Point out each Plasmodium parasite.
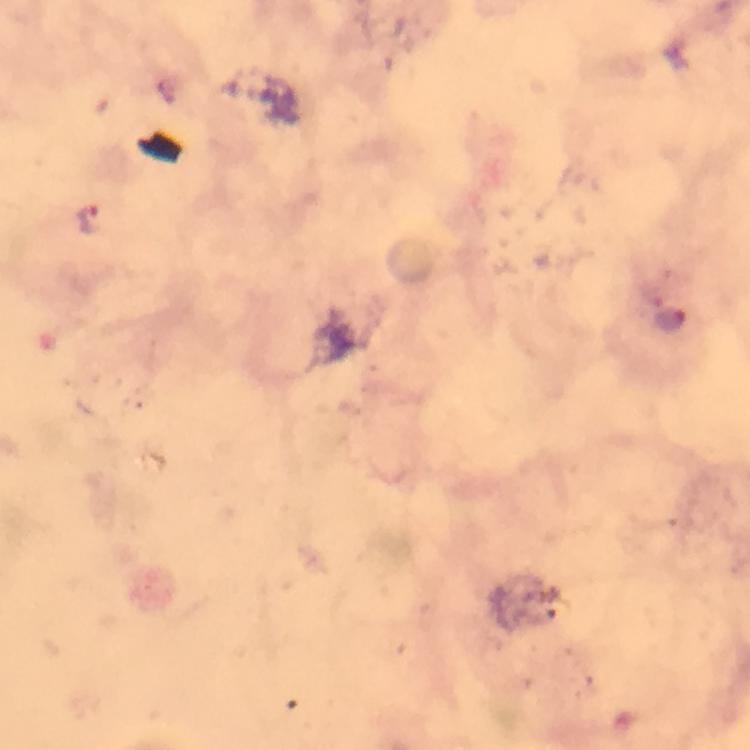

Approximate object centers, in pixels from the top-left corner.
Plasmodium parasites: (x=91, y=220), (x=673, y=322).

stain = Giemsa
image size = 750×750 pixels
immersion oil = used
preparation = thick blood smear
capture = smartphone mounted on the microscope
cropped from = one field of view
magnification = 100x
context = from a diagnostic examination for malaria